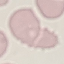

result: negative for malaria parasites
image_type: automatically extracted cell patch, resized to 64 × 64 pixels
stain: Giemsa
preparation: thin smear
capture: smartphone through the microscope eyepiece